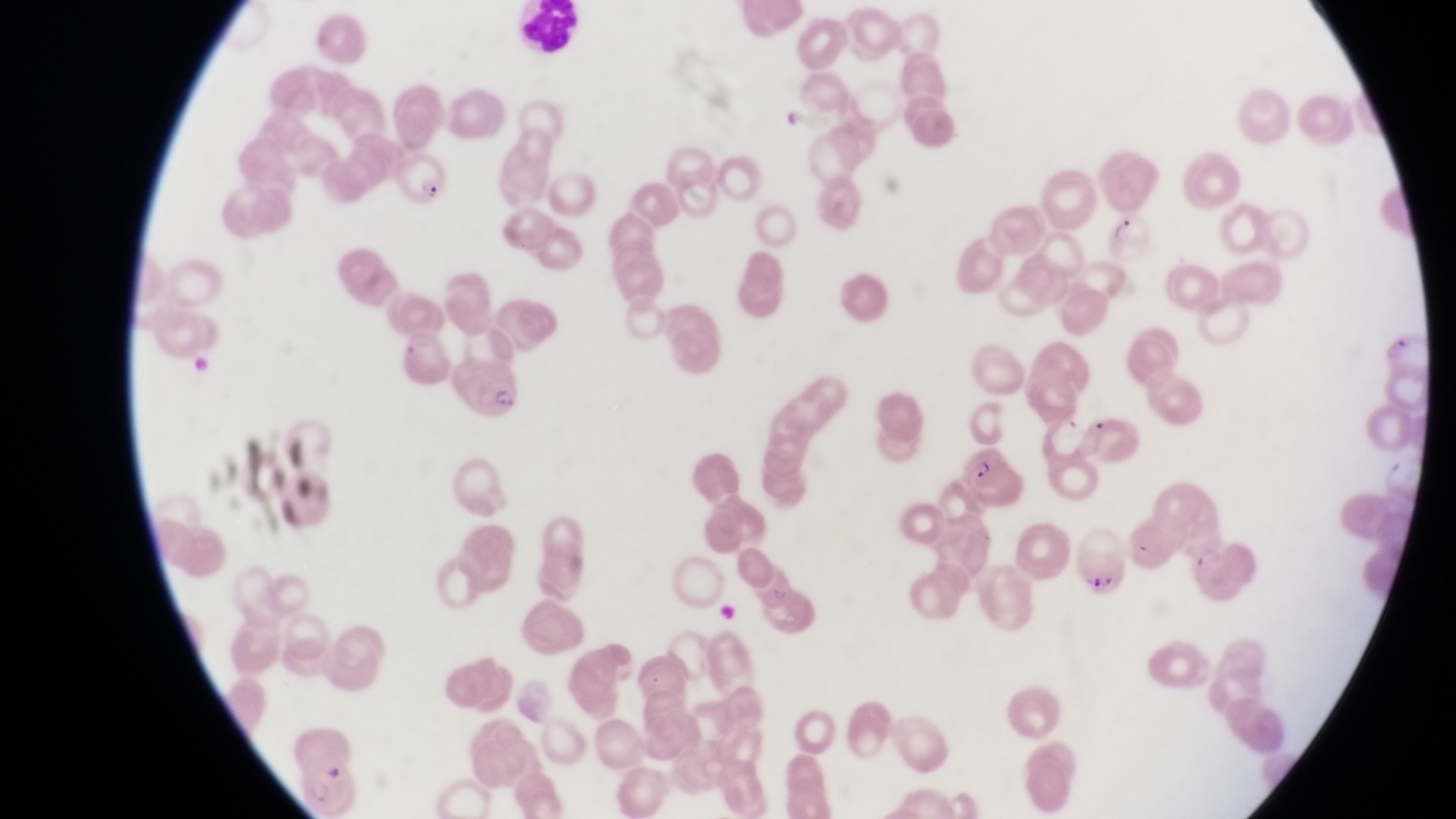
parasitised red blood cell locations = approximate bounding boxes as {left, top, right, bottom} in pixels: {396, 143, 445, 203}, {1106, 206, 1155, 267}, {453, 354, 517, 420}, {957, 446, 1028, 507}
artifact (platelet-like body, stain precipitate, or debris) locations = approximate bounding boxes as {left, top, right, bottom} in pixels: {1068, 523, 1141, 592}
image size = 1456×819 pixels
field of view = single
capture = smartphone photograph through the eyepiece of an Olympus CX-23 microscope
magnification = 1000x
country = Uganda
preparation = thin blood smear